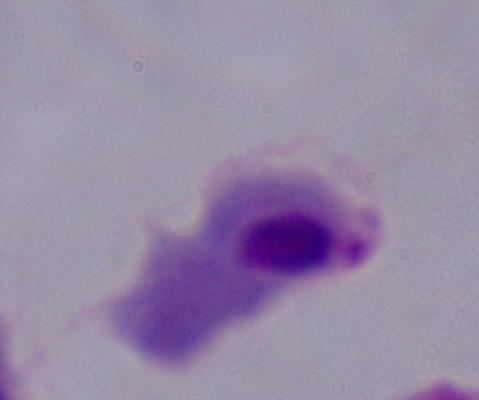

A trichomonad is shown. Micrograph. 1000x magnification.